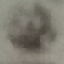

Summary:
  - Result: no malaria parasites seen
  - Preparation: thin blood smear
  - Capture: smartphone camera at the microscope eyepiece
  - Stain: Giemsa
  - Image type: automatically extracted cell patch, resized to 64 × 64 pixels